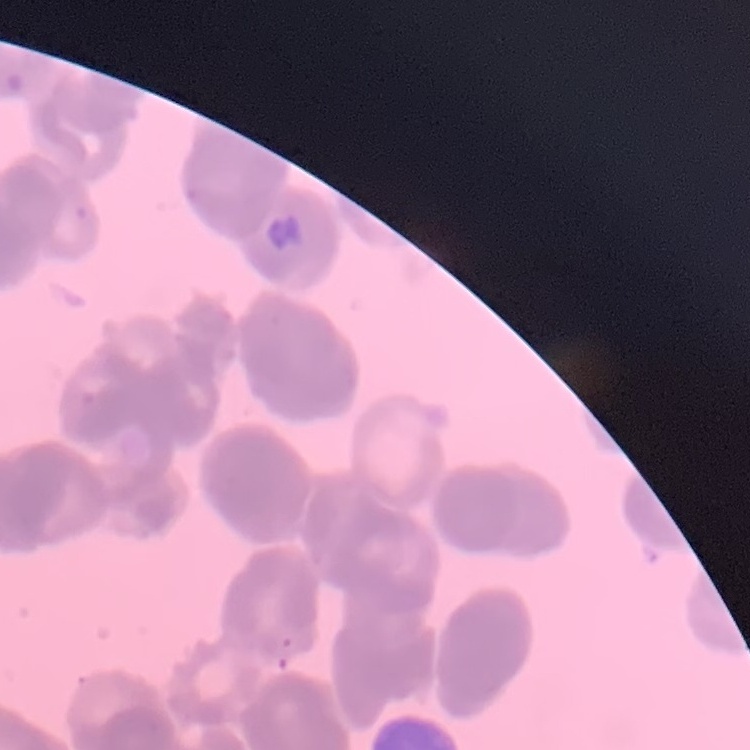

red blood cell morphology = rouleaux formation
image type = square crop of a larger photomicrograph
stain = Field's or Giemsa
preparation = thin peripheral smear